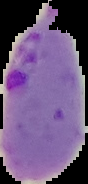
Summary:
  - Result: malaria parasites identified
  - Preparation: thin blood film
  - Image size: 88×184 pixels
  - Image type: segmented cell region with the area outside set to black